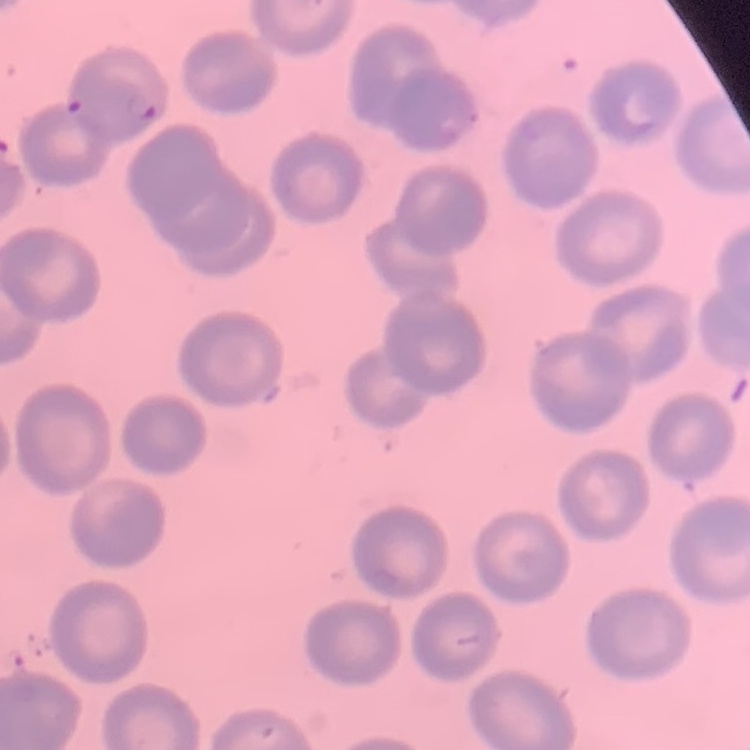
The red blood cells exhibit no rouleaux formation. Stained with either Field's or Giemsa. Thin blood film. One tile cut from a larger photomicrograph.